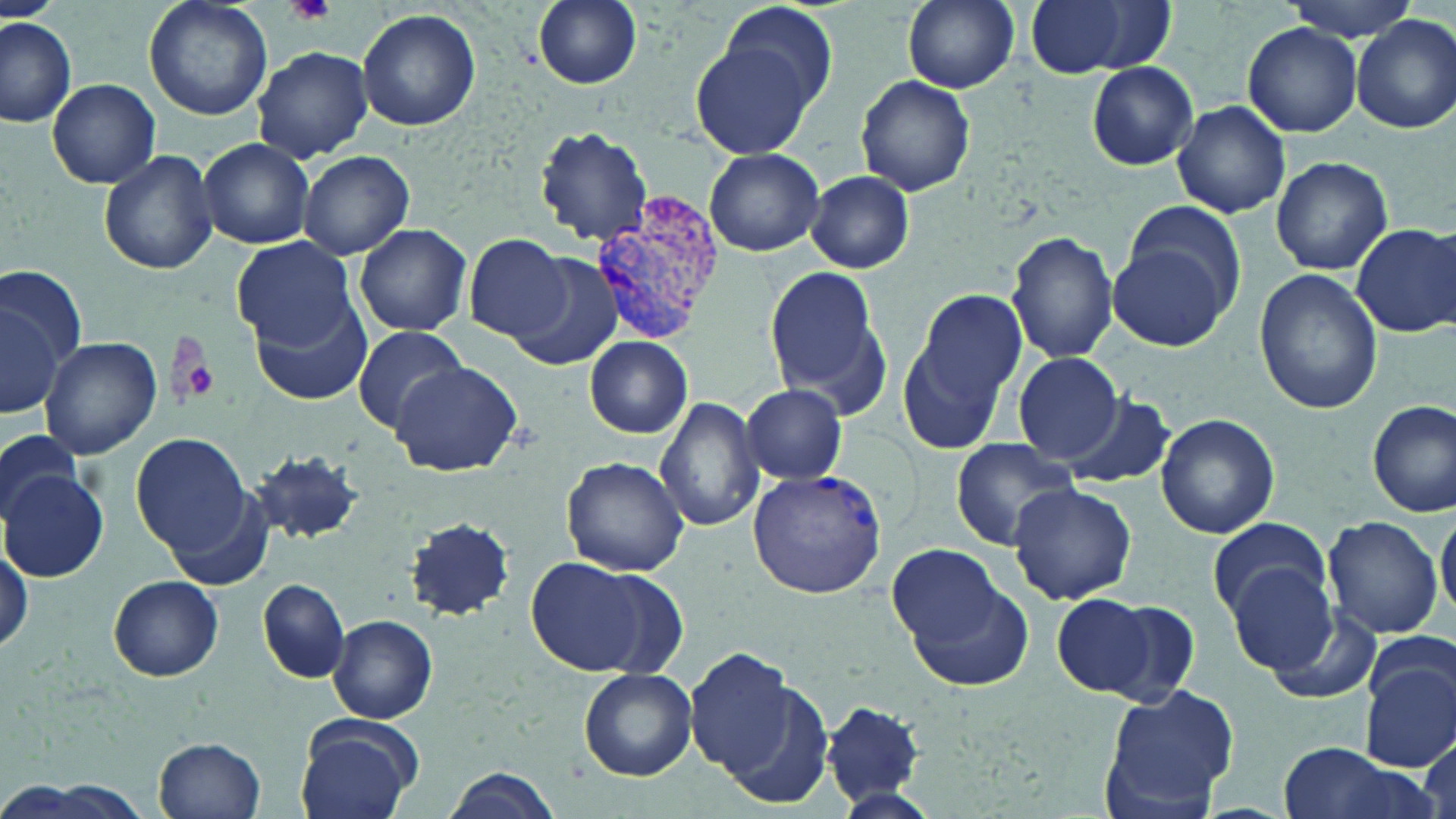

Summary:
  - Coordinate format: approximate bounding boxes as (x1, y1, x2, y2) in pixels
  - Plasmodium vivax-infected red blood cell locations: (586, 192, 728, 341), (748, 468, 888, 596)
  - Platelet locations: (284, 0, 337, 25), (175, 338, 222, 406)
  - Uninfected red blood cell locations: (145, 0, 271, 121), (531, 0, 642, 89), (901, 0, 1021, 92), (1025, 0, 1174, 80), (1282, 0, 1423, 42), (715, 1, 839, 120), (357, 7, 481, 133), (0, 15, 78, 127), (1352, 15, 1456, 133), (1242, 23, 1360, 135), (691, 40, 817, 159), (251, 46, 372, 163), (1086, 62, 1198, 169), (857, 74, 976, 197), (48, 78, 160, 188), (1171, 100, 1290, 218), (535, 126, 653, 245), (198, 138, 315, 248), (703, 147, 825, 257), (98, 149, 219, 275), (296, 149, 415, 260), (1270, 155, 1393, 276), (805, 171, 914, 273), (1127, 203, 1247, 317), (353, 222, 472, 337), (1352, 223, 1456, 337), (1006, 231, 1120, 363), (465, 234, 572, 341), (231, 236, 356, 348), (1108, 238, 1233, 352), (501, 247, 624, 368), (764, 262, 890, 415), (0, 267, 85, 380), (1253, 269, 1383, 415), (897, 287, 1028, 456), (249, 294, 370, 406), (2, 301, 66, 419), (352, 325, 468, 432), (38, 336, 162, 460), (585, 337, 693, 439), (1013, 351, 1125, 463), (389, 359, 522, 477), (740, 384, 846, 485), (1058, 394, 1176, 492), (655, 396, 766, 535), (1368, 398, 1455, 516), (1155, 412, 1281, 540), (0, 429, 82, 524), (133, 433, 252, 555), (949, 436, 1080, 550), (249, 448, 365, 543), (560, 457, 688, 576), (2, 470, 110, 581), (1008, 483, 1137, 606), (161, 484, 278, 590), (1437, 505, 1455, 625), (1320, 515, 1445, 640), (404, 517, 513, 620), (1208, 517, 1331, 619), (0, 534, 32, 658), (887, 545, 1010, 650), (527, 556, 670, 675), (1223, 562, 1341, 675), (906, 572, 1035, 693), (109, 576, 224, 680), (258, 579, 350, 683), (1058, 596, 1187, 701), (1260, 602, 1385, 708), (329, 614, 437, 723), (684, 648, 797, 777), (1358, 655, 1456, 772), (580, 668, 697, 780), (719, 678, 835, 808), (1098, 683, 1242, 818), (824, 700, 926, 806), (295, 716, 420, 819), (1416, 734, 1454, 819), (155, 736, 267, 819), (1276, 743, 1423, 819), (440, 768, 566, 819)
  - Slide-level diagnosis: Plasmodium vivax
  - Field of view: single
  - Modality: light microscopy
  - Magnification: 1000x
  - Stain: May-Grünwald-Giemsa
  - Preparation: thin blood film
  - Image size: 1456×819 pixels